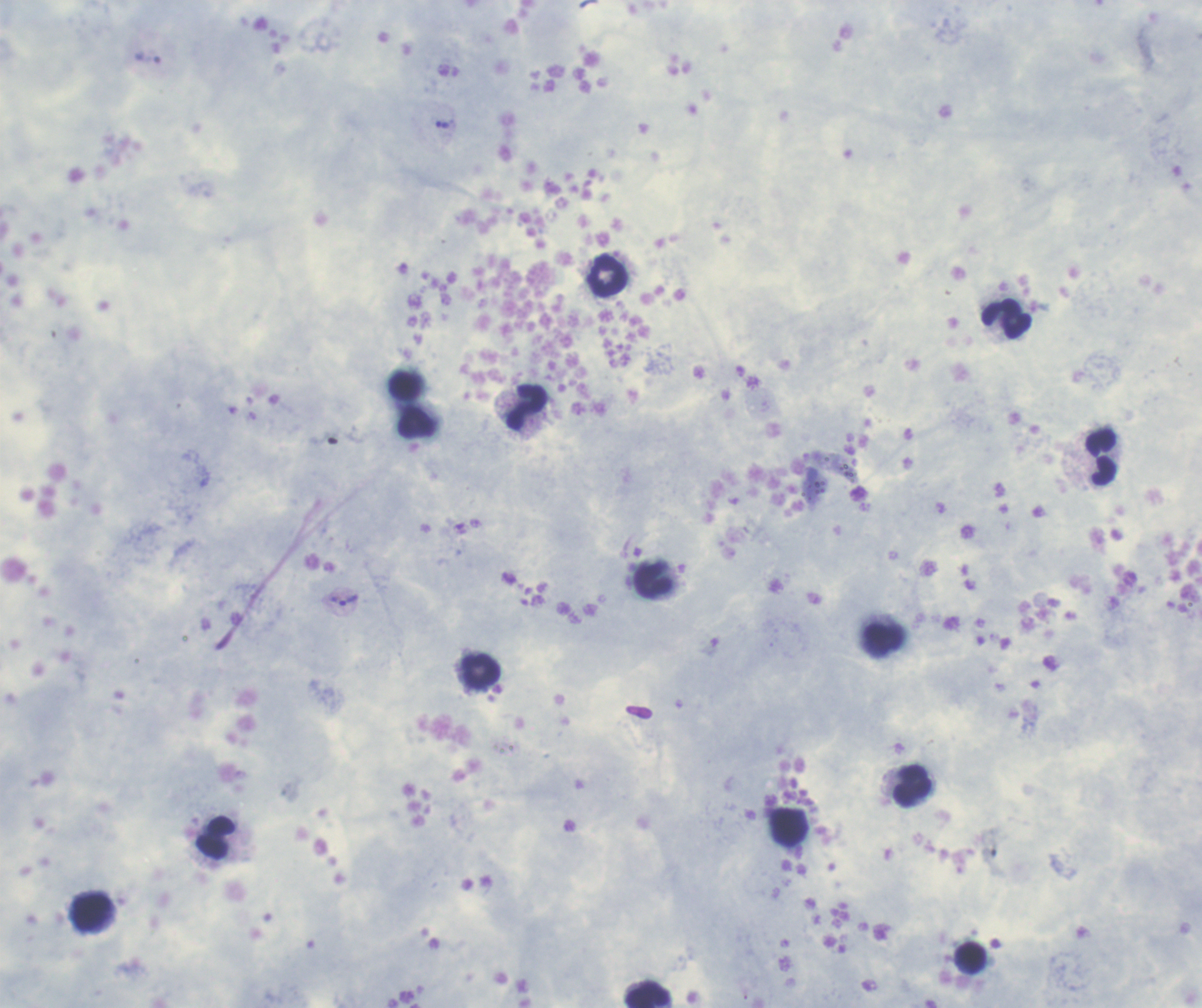 Coloration quality: good. Romanowsky stain. Image is 1202×1008 pixels. Single field of view. Thick smear of blood.